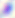
{
  "modality": "photomicrograph",
  "magnification": "400x",
  "identification": "Toxoplasma gondii"
}